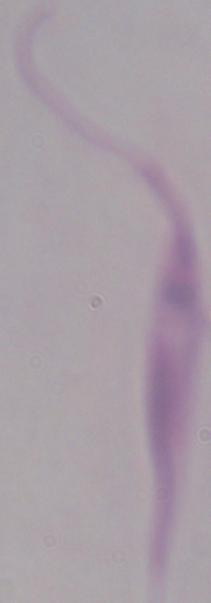
modality = micrograph
identification = Leishmania
magnification = 1000x